Locate every leukocyte (white blood cell).
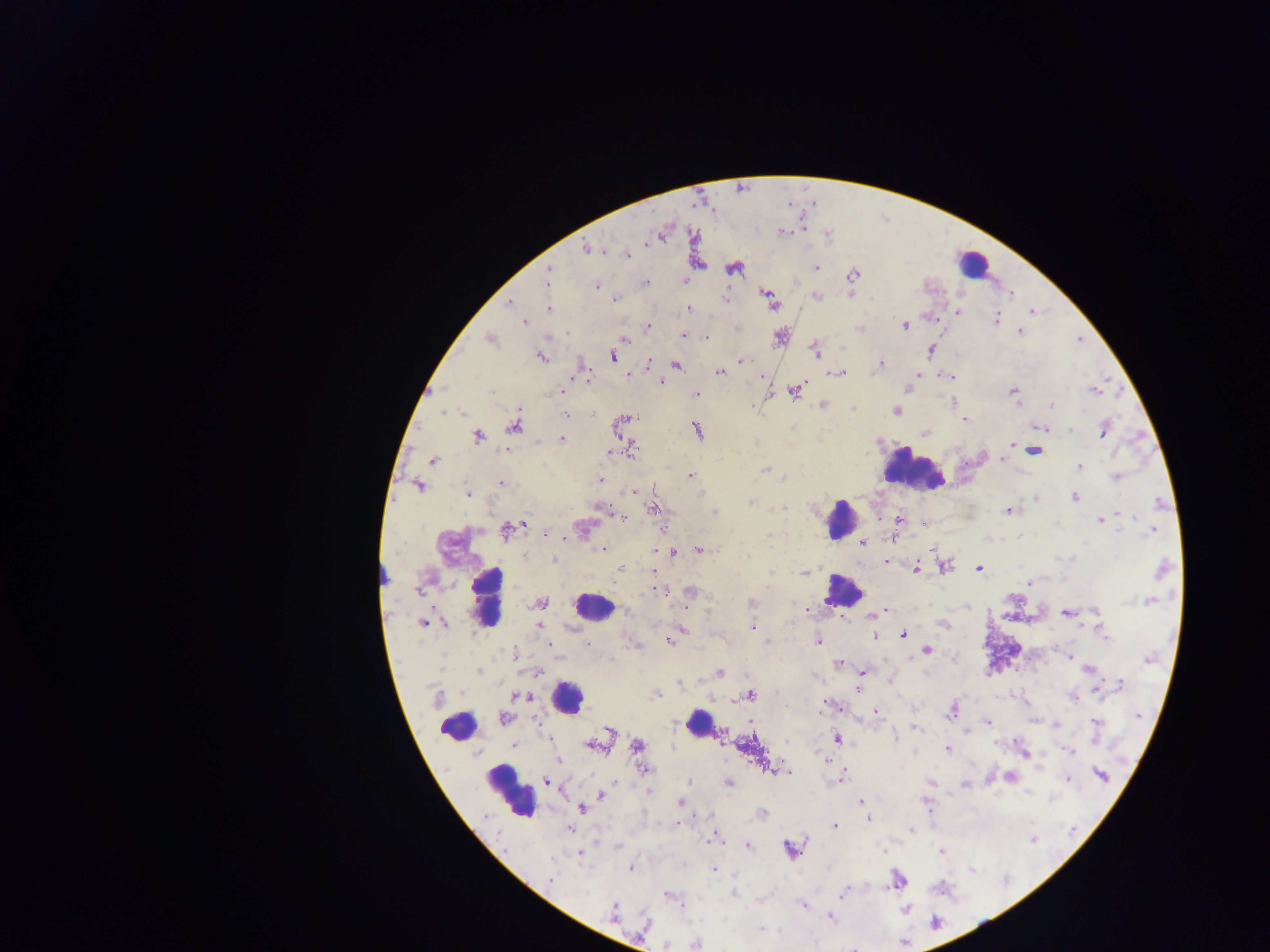

Approximate centers as (x, y) in pixels.
Leukocytes: (973, 264), (914, 472), (841, 518), (384, 573), (842, 591), (488, 597), (593, 606), (566, 696), (699, 724), (457, 726), (509, 792).

Malaria parasite locations: (783, 232), (586, 247), (627, 254), (816, 268), (733, 269), (549, 270), (853, 275), (546, 279), (644, 283), (597, 285), (817, 295), (767, 296), (726, 298), (615, 299), (871, 299), (509, 302), (549, 308), (689, 309), (1032, 311), (957, 312), (996, 318), (524, 323), (905, 325), (649, 326), (860, 329), (1020, 332), (684, 335), (779, 337), (705, 338), (491, 339), (624, 339), (814, 350), (931, 350), (541, 356), (612, 356), (741, 361), (648, 364), (676, 364), (881, 364), (582, 367), (720, 372), (839, 373), (628, 374), (918, 374), (949, 377), (661, 382), (561, 389), (909, 389), (794, 390), (1094, 390), (1013, 391), (696, 395), (954, 400), (823, 404), (1052, 405), (896, 411), (443, 413), (461, 413), (566, 415), (626, 418), (965, 420), (622, 423), (513, 426), (1041, 428), (697, 430), (1070, 430), (1104, 431), (926, 432), (478, 436), (561, 438), (539, 441), (1011, 445), (506, 449), (631, 450), (1035, 450), (612, 451), (1002, 459), (432, 460), (1080, 467), (765, 469), (690, 476), (1116, 476), (601, 481), (501, 482), (419, 486), (631, 491), (468, 494), (1036, 497), (1075, 497), (750, 502), (782, 507), (599, 509), (654, 509), (714, 511), (1008, 511), (1120, 514), (622, 516), (899, 520), (1101, 521), (926, 524), (518, 525), (583, 528), (1152, 530), (507, 531), (547, 533), (891, 539), (863, 543), (603, 548), (698, 549), (672, 553), (524, 557), (748, 557), (554, 560), (886, 562), (944, 566), (916, 568), (979, 569), (1162, 569), (620, 570), (654, 572), (770, 572), (805, 572), (1030, 582), (657, 589), (418, 590), (690, 592), (752, 602), (1148, 602), (542, 603), (686, 607), (627, 611), (875, 613), (1066, 613), (1096, 613), (944, 623), (423, 624), (444, 624), (539, 626), (753, 627), (682, 631), (1104, 634), (876, 635), (903, 635), (676, 636), (670, 641), (766, 641), (818, 641), (587, 644), (550, 645), (927, 650), (514, 652), (1069, 657), (955, 659), (1149, 659), (839, 663), (1088, 669), (479, 671), (537, 672), (862, 672), (719, 673), (679, 684), (1120, 685), (857, 688), (654, 695), (750, 695), (521, 696), (1074, 697), (824, 706), (952, 711), (876, 712), (1139, 717), (504, 718), (988, 722), (1096, 723), (1056, 726), (917, 728), (611, 732), (894, 737), (837, 739), (513, 745), (593, 745), (637, 745), (947, 749), (1069, 750), (559, 761), (644, 769), (778, 769), (788, 771), (1101, 776), (840, 777), (1010, 777), (1068, 779), (547, 781), (689, 781), (930, 781), (729, 783), (964, 784), (601, 795), (680, 802), (861, 802), (926, 803), (582, 808), (761, 813), (869, 819), (835, 825), (569, 829), (911, 829), (712, 839), (748, 845), (790, 850), (941, 852), (580, 854), (551, 860), (630, 868), (714, 869), (549, 879), (897, 880), (734, 893), (842, 894), (669, 896), (803, 905), (905, 910), (613, 911), (830, 918), (761, 929), (695, 943), (666, 945). One field of view. Thick blood smear. Collected in Ghana. Photographed through a microscope with a mobile-phone camera. Image is 1270×952 pixels.